Point out leukocytes.
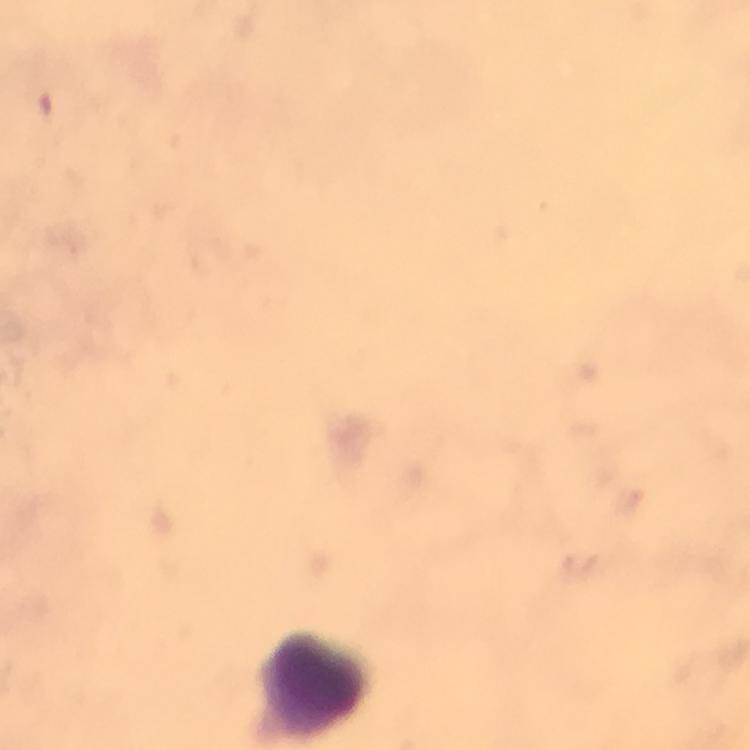
Approximate centers as {x, y} in pixels.
Leukocytes: {315, 684}.

Plasmodium parasites = none detected
image size = 750×750 pixels
cropped from = a single field of view
preparation = thick blood smear
capture = smartphone camera through the microscope
stain = Giemsa
immersion oil = used
context = from a malaria diagnostic workup
magnification = 100x